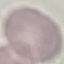

malaria status = uninfected
capture = smartphone through the microscope eyepiece
stain = Giemsa
image type = automatically extracted cell patch, resized to 64 × 64 pixels
preparation = thin blood film